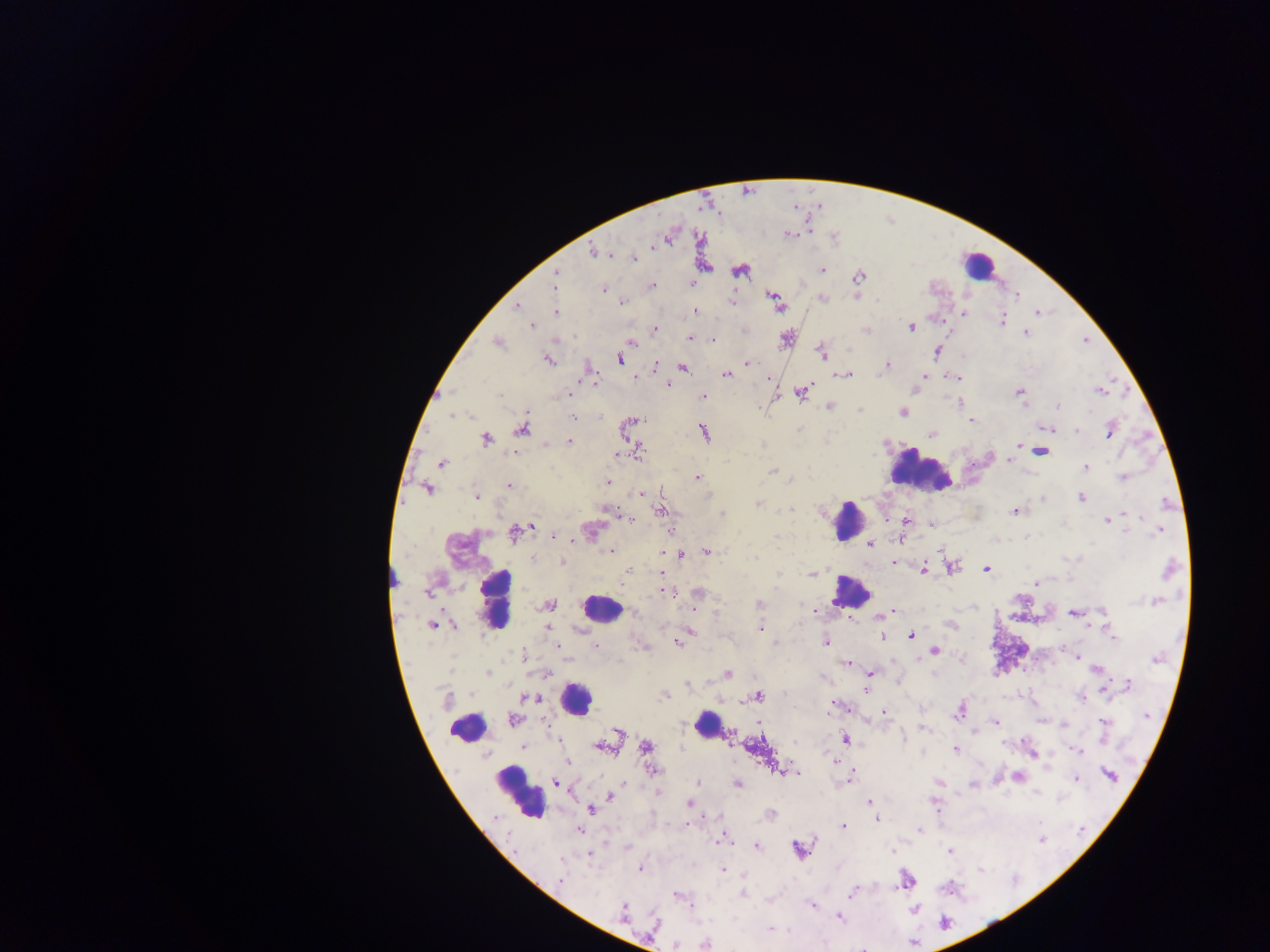 Approximate centers as {x, y} in pixels. Malaria parasite locations: {788, 234}, {666, 236}, {593, 252}, {612, 254}, {634, 257}, {704, 265}, {739, 269}, {821, 270}, {555, 274}, {858, 276}, {691, 282}, {555, 284}, {652, 284}, {604, 289}, {1017, 296}, {857, 297}, {774, 298}, {822, 298}, {732, 301}, {623, 302}, {517, 307}, {694, 311}, {556, 312}, {964, 312}, {1037, 312}, {1002, 320}, {942, 321}, {532, 325}, {911, 327}, {654, 329}, {866, 329}, {1025, 332}, {690, 338}, {787, 338}, {712, 339}, {497, 341}, {631, 342}, {936, 351}, {822, 353}, {619, 358}, {548, 360}, {747, 364}, {886, 365}, {655, 366}, {682, 368}, {726, 374}, {845, 374}, {924, 375}, {635, 376}, {767, 377}, {920, 377}, {955, 377}, {594, 381}, {667, 383}, {1099, 390}, {801, 391}, {915, 391}, {1020, 392}, {569, 393}, {702, 396}, {961, 401}, {830, 406}, {1058, 407}, {860, 408}, {902, 412}, {574, 417}, {971, 419}, {627, 426}, {1046, 427}, {522, 428}, {1110, 429}, {1076, 431}, {704, 432}, {931, 433}, {485, 439}, {568, 441}, {1019, 444}, {636, 451}, {1040, 451}, {615, 455}, {1009, 459}, {442, 463}, {1086, 468}, {772, 471}, {696, 478}, {1124, 478}, {607, 482}, {509, 485}, {427, 488}, {641, 493}, {476, 496}, {1043, 496}, {1082, 497}, {757, 502}, {606, 508}, {661, 510}, {1015, 511}, {721, 513}, {630, 518}, {1107, 519}, {906, 521}, {932, 525}, {531, 527}, {590, 530}, {1160, 530}, {671, 531}, {516, 532}, {553, 535}, {870, 543}, {942, 550}, {609, 551}, {706, 551}, {662, 552}, {680, 554}, {535, 559}, {562, 561}, {892, 561}, {951, 567}, {1169, 568}, {629, 569}, {987, 569}, {922, 570}, {662, 573}, {813, 574}, {1036, 582}, {623, 583}, {665, 592}, {698, 593}, {1155, 601}, {548, 605}, {758, 605}, {694, 606}, {813, 611}, {892, 611}, {1074, 613}, {849, 618}, {950, 623}, {434, 624}, {547, 627}, {759, 629}, {689, 631}, {910, 635}, {882, 636}, {1113, 638}, {679, 640}, {826, 641}, {596, 645}, {557, 646}, {644, 646}, {934, 651}, {523, 656}, {1077, 656}, {846, 663}, {1096, 669}, {487, 671}, {870, 672}, {546, 674}, {727, 674}, {686, 684}, {1127, 684}, {866, 688}, {1105, 689}, {664, 695}, {757, 696}, {1081, 696}, {525, 697}, {532, 698}, {959, 710}, {884, 711}, {514, 720}, {996, 723}, {1063, 724}, {1104, 725}, {923, 729}, {618, 731}, {729, 734}, {844, 738}, {558, 741}, {523, 746}, {602, 746}, {646, 747}, {955, 749}, {1079, 751}, {1032, 753}, {836, 762}, {651, 771}, {784, 772}, {798, 772}, {851, 773}, {1108, 774}, {1018, 777}, {849, 778}, {1075, 779}, {939, 781}, {556, 782}, {622, 782}, {697, 783}, {737, 783}, {972, 784}, {657, 792}, {610, 796}, {869, 802}, {689, 803}, {934, 804}, {590, 808}, {770, 814}, {876, 819}, {843, 826}, {578, 829}, {918, 829}, {722, 838}, {756, 846}, {799, 849}, {949, 850}, {892, 852}, {589, 854}, {639, 868}, {722, 869}, {905, 880}, {560, 881}, {742, 891}, {854, 892}, {677, 896}, {813, 905}, {914, 909}, {623, 913}, {838, 916}, {653, 925}, {705, 944}. Leukocyte locations: {977, 265}, {917, 471}, {848, 520}, {390, 577}, {851, 592}, {494, 598}, {601, 610}, {574, 699}, {707, 723}, {467, 727}, {519, 793}. One field of view. Mobile-phone photograph taken through the microscope. Thick blood smear. Sample from Ghana. Image is 1270×952 pixels.